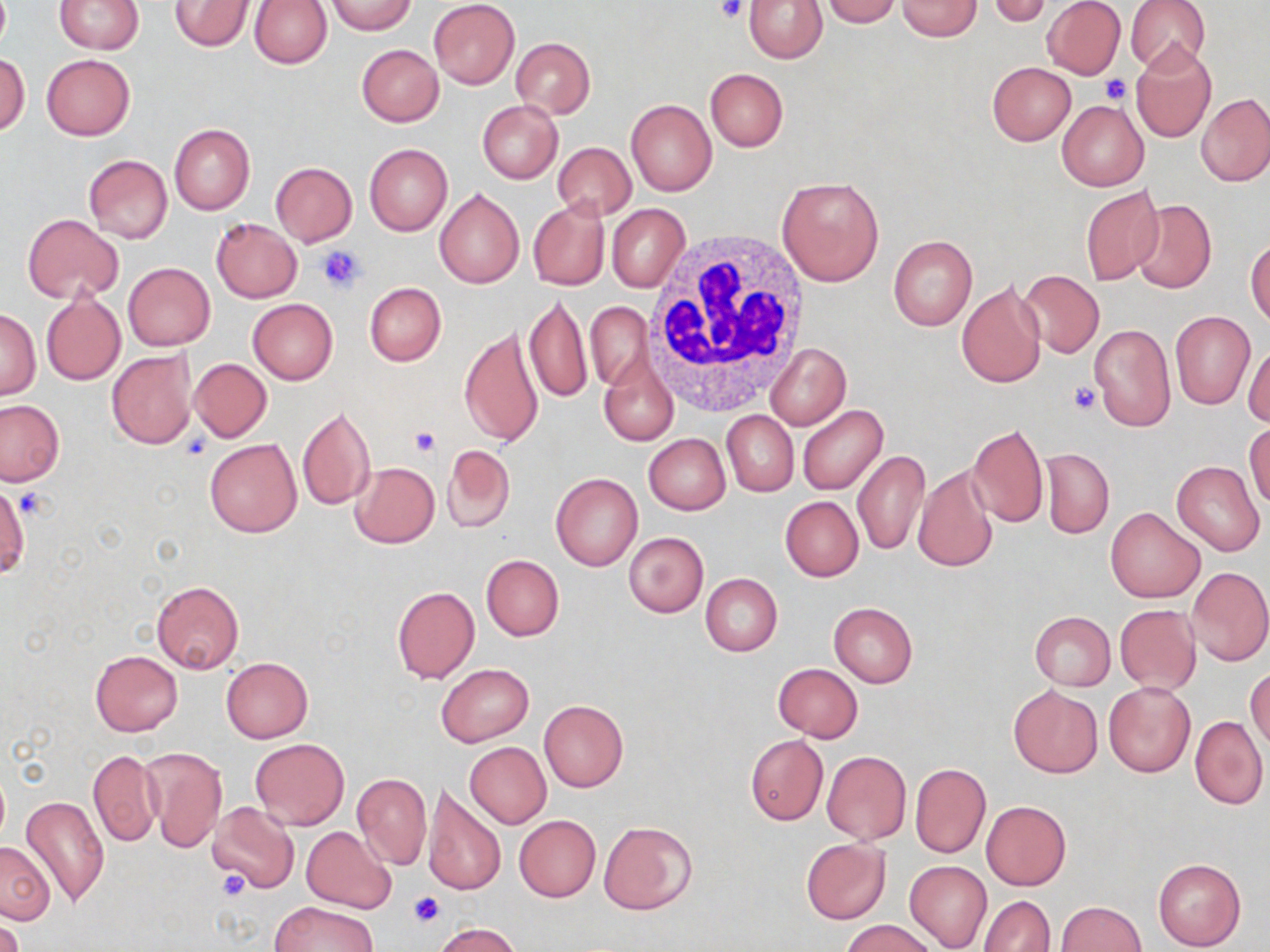
slide-level diagnosis = negative for blood parasites
platelet locations = approximate bounding boxes as (x1,y1)-(x2,y2) corner pairs in pixels: (715,0)-(746,23), (1099,75)-(1130,104), (318,245)-(368,292), (1069,381)-(1099,415), (410,425)-(440,457), (180,432)-(211,462), (15,489)-(50,519), (218,870)-(250,899), (408,890)-(444,926)
modality = light microscopy
stain = May-Grünwald-Giemsa
preparation = thin blood smear
field of view = one of a larger specimen
uninfected red blood cell locations = approximate bounding boxes as (x1,y1)-(x2,y2) corner pairs in pixels: (170,0)-(254,51), (428,0)-(520,88), (743,0)-(829,63), (821,0)-(900,26), (1042,0)-(1126,79), (1124,0)-(1210,74), (54,1)-(144,54), (248,1)-(332,68), (325,1)-(416,34), (896,1)-(982,40), (988,1)-(1055,27), (511,37)-(595,119), (1131,43)-(1217,144), (356,44)-(444,126), (1,52)-(30,136), (42,54)-(136,140), (986,61)-(1076,146), (705,68)-(788,151), (1197,93)-(1270,186), (626,99)-(716,195), (1057,99)-(1149,191), (477,100)-(563,184), (169,123)-(255,215), (553,142)-(636,220), (364,144)-(453,236), (84,154)-(172,244), (271,162)-(357,245), (776,175)-(886,287), (1080,185)-(1165,286), (434,187)-(524,289), (527,198)-(609,292), (1130,199)-(1217,296), (607,204)-(689,293), (22,214)-(123,303), (211,218)-(302,302), (888,236)-(977,330), (1247,237)-(1270,326), (123,262)-(215,350), (1016,270)-(1105,357), (956,280)-(1046,388), (364,282)-(446,366), (41,293)-(126,386), (524,294)-(592,406), (247,299)-(337,385), (585,301)-(652,391), (0,309)-(40,399), (1170,311)-(1255,409), (1089,322)-(1175,433), (459,326)-(544,450), (1243,341)-(1270,427), (765,342)-(849,430), (106,349)-(198,450), (599,353)-(679,446), (190,358)-(271,442), (0,401)-(64,485), (296,404)-(375,511), (797,404)-(888,495), (721,410)-(798,497), (1246,423)-(1270,509), (967,425)-(1049,528), (644,434)-(730,514), (204,438)-(302,536), (442,444)-(514,533), (1041,448)-(1114,539), (852,450)-(930,556), (350,461)-(440,548), (1171,461)-(1265,558), (913,464)-(999,573), (551,472)-(643,572), (0,484)-(28,577), (780,496)-(863,581), (1106,507)-(1204,603), (624,533)-(709,617), (480,554)-(564,641), (1187,566)-(1270,666), (700,573)-(783,657), (151,580)-(244,674), (391,586)-(479,684), (829,603)-(918,688), (1115,604)-(1201,694), (1029,612)-(1115,690), (90,651)-(182,736), (222,656)-(313,742), (435,662)-(534,747), (773,663)-(863,741), (1246,665)-(1270,752), (1103,682)-(1196,778), (1008,685)-(1102,777), (539,700)-(629,793), (1190,716)-(1268,811), (745,735)-(829,825), (250,737)-(348,831), (465,743)-(551,829), (141,746)-(226,853), (87,749)-(163,846), (821,750)-(911,845), (910,764)-(990,858), (352,772)-(432,869), (423,784)-(506,897), (21,793)-(110,909), (981,800)-(1072,890), (206,802)-(300,895), (513,815)-(601,901), (599,819)-(698,916), (302,826)-(396,912), (800,839)-(891,925), (0,840)-(55,924), (1152,857)-(1247,952), (904,861)-(992,952), (979,895)-(1056,952), (270,901)-(378,952), (1057,901)-(1145,952), (0,917)-(24,952), (841,919)-(937,952), (430,921)-(523,951)
white blood cell locations = approximate bounding boxes as (x1,y1)-(x2,y2) corner pairs in pixels: (646,231)-(814,408)
image size = 1270×952 pixels
magnification = 1000x